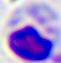
magnification = 400x
identification = leukocyte
modality = micrograph